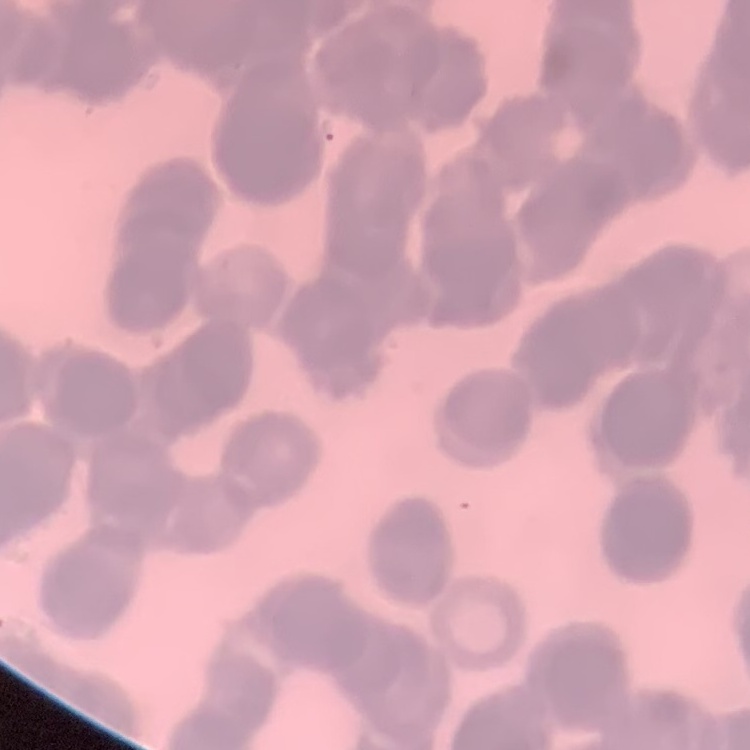
Summary:
  - Erythrocyte morphology: rouleaux formation
  - Preparation: thin peripheral smear
  - Stain: Field's or Giemsa
  - Image type: square crop of a larger photomicrograph